Assess this cell for malaria.
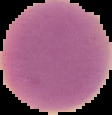
Uninfected.

From a thin blood smear. Cell region segmented out of the field of view; the surrounding area is masked to black. Image is 112×115 pixels.